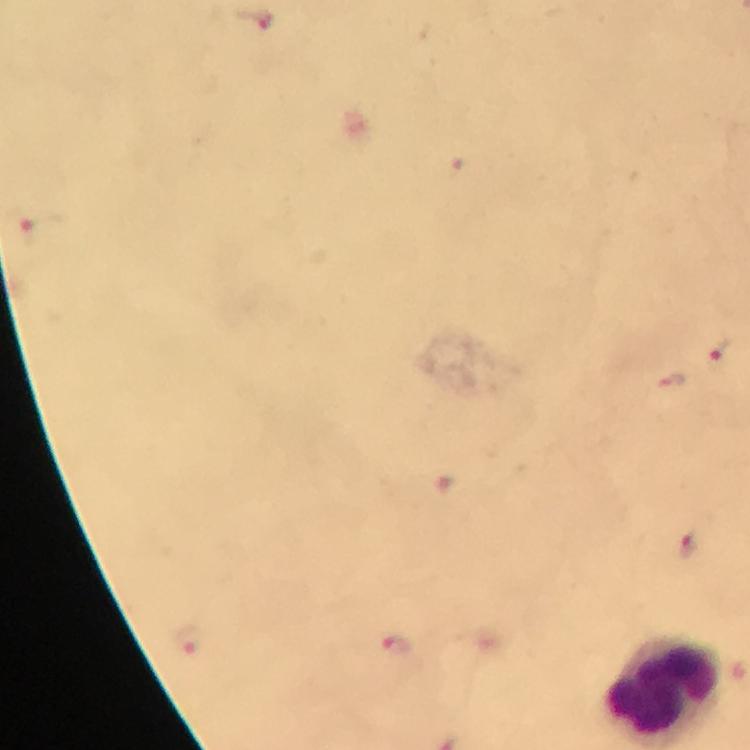

Approximate centers as {x, y} in pixels. Plasmodium parasite locations: {256, 21}, {720, 348}, {687, 542}, {187, 642}, {396, 649}. Immersion oil applied. From a malaria diagnostic workup. Photographed through the microscope with a smartphone camera. Image is 750×750 pixels. Cropped region of a single field of view. Giemsa stain. Thick blood film. 100x magnification.